Identify the blood parasite species.
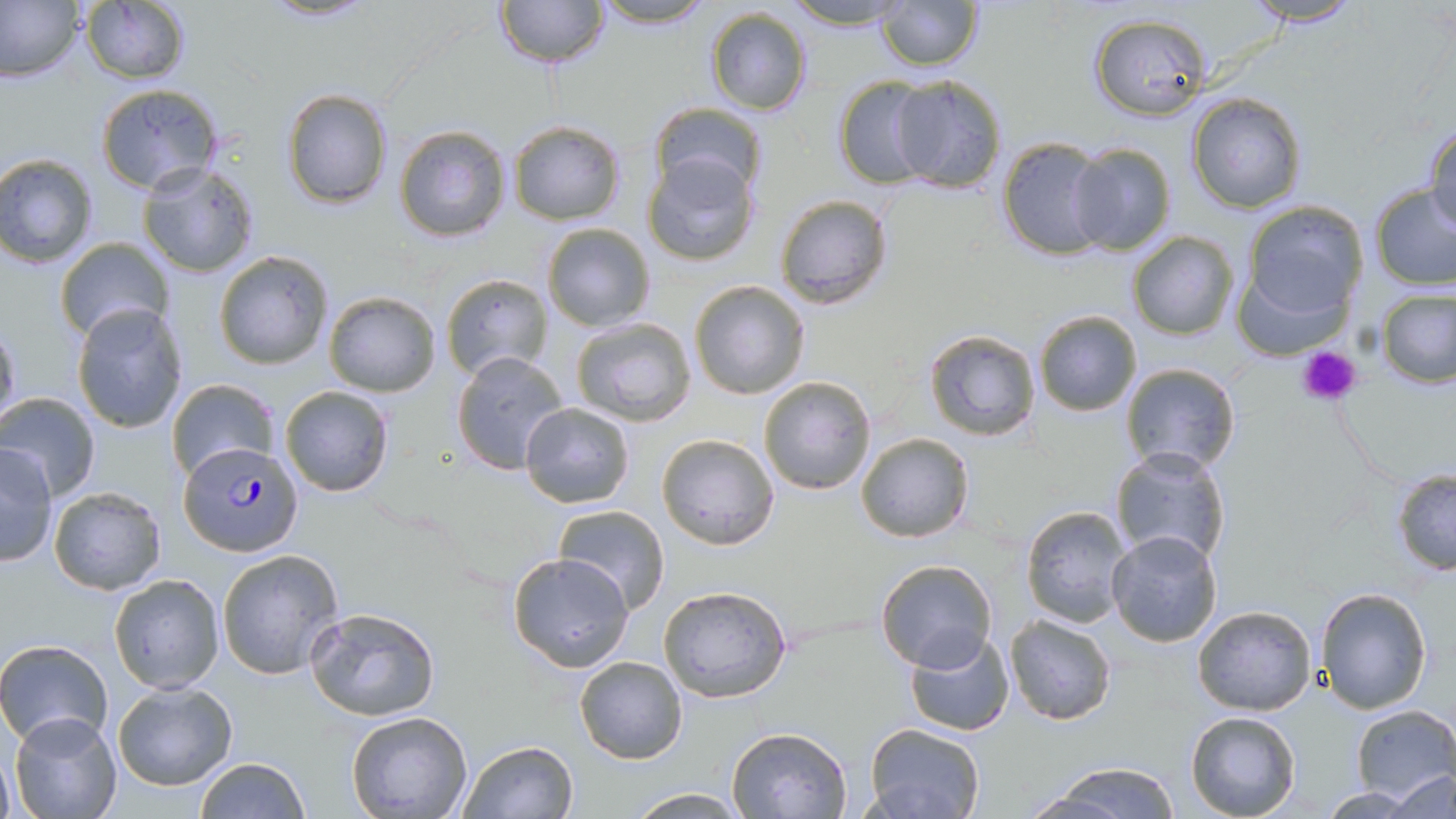

Plasmodium falciparum.

Approximate bounding boxes as (x1,y1)-(x2,y2) corner pairs in pixels. Plasmodium falciparum-infected red blood cell locations: (179,442)-(302,558). Platelet locations: (1297,345)-(1362,409). Uninfected red blood cell locations: (259,0)-(378,23), (493,0)-(610,69), (592,0)-(718,29), (781,0)-(915,30), (876,0)-(984,71), (1239,0)-(1368,27), (0,1)-(84,82), (79,3)-(190,83), (704,7)-(813,115), (1087,13)-(1212,121), (888,75)-(1008,194), (832,76)-(937,188), (97,84)-(222,194), (281,89)-(392,208), (1186,93)-(1306,212), (650,102)-(768,200), (508,120)-(625,225), (394,124)-(511,242), (1424,127)-(1455,233), (996,135)-(1114,261), (1067,142)-(1178,254), (641,150)-(761,266), (0,153)-(98,269), (138,161)-(258,277), (1370,184)-(1456,289), (773,194)-(893,311), (1240,200)-(1369,325), (540,222)-(656,331), (1128,231)-(1237,339), (54,236)-(175,343), (213,250)-(334,370), (441,273)-(554,382), (690,280)-(810,400), (1377,288)-(1455,389), (323,290)-(442,397), (71,305)-(187,431), (1033,310)-(1141,416), (569,317)-(698,426), (0,318)-(20,429), (921,328)-(1042,444), (449,350)-(572,477), (1119,363)-(1241,475), (758,375)-(876,495), (166,379)-(278,481), (279,385)-(394,497), (0,392)-(101,499), (520,402)-(635,508), (856,431)-(975,544), (657,433)-(781,551), (1,444)-(59,567), (1110,446)-(1233,567), (1391,469)-(1455,575), (47,487)-(167,596), (554,505)-(671,613), (1020,505)-(1135,628), (1104,529)-(1223,649), (218,550)-(347,679), (506,552)-(635,674), (875,559)-(998,672), (110,573)-(224,692), (658,584)-(792,703), (1316,588)-(1433,713), (304,605)-(441,723), (1191,605)-(1317,715), (1005,615)-(1117,726), (903,631)-(1015,736), (0,639)-(113,749), (573,655)-(687,764), (111,681)-(238,791), (1351,705)-(1456,800), (346,709)-(473,818), (10,710)-(123,817), (1184,710)-(1301,819), (863,722)-(983,819), (727,725)-(852,817), (457,740)-(579,819), (193,756)-(309,819), (1032,761)-(1186,818), (1383,768)-(1455,818), (625,788)-(746,817). 1000x magnification. Single field of view. Thin blood smear. Image is 1456×819 pixels. Light microscopy. May-Grünwald-Giemsa stain.